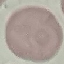
{
  "malaria_status": "uninfected",
  "capture": "smartphone camera at the microscope eyepiece",
  "stain": "Giemsa",
  "preparation": "thin blood film",
  "image_type": "cell patch, automatically extracted from a larger field of view and resized to 64 × 64 pixels"
}